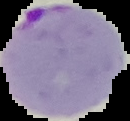 Result: malaria parasites detected. Image is 130×121 pixels. Segmented cell region on a black background. From a thin blood film.